Report the malaria status of this cell.
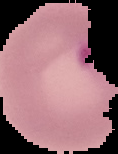

Parasitized.

Summary:
  - Image type: segmented cell region with the area outside set to black
  - Preparation: thin blood smear
  - Image size: 118×154 pixels